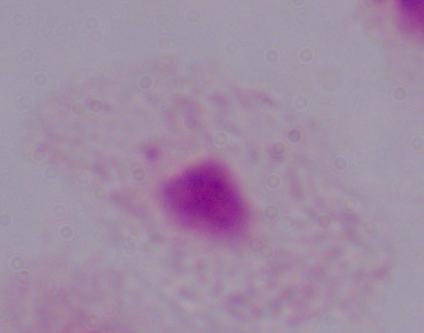
identification = trichomonad
magnification = 1000x
modality = micrograph